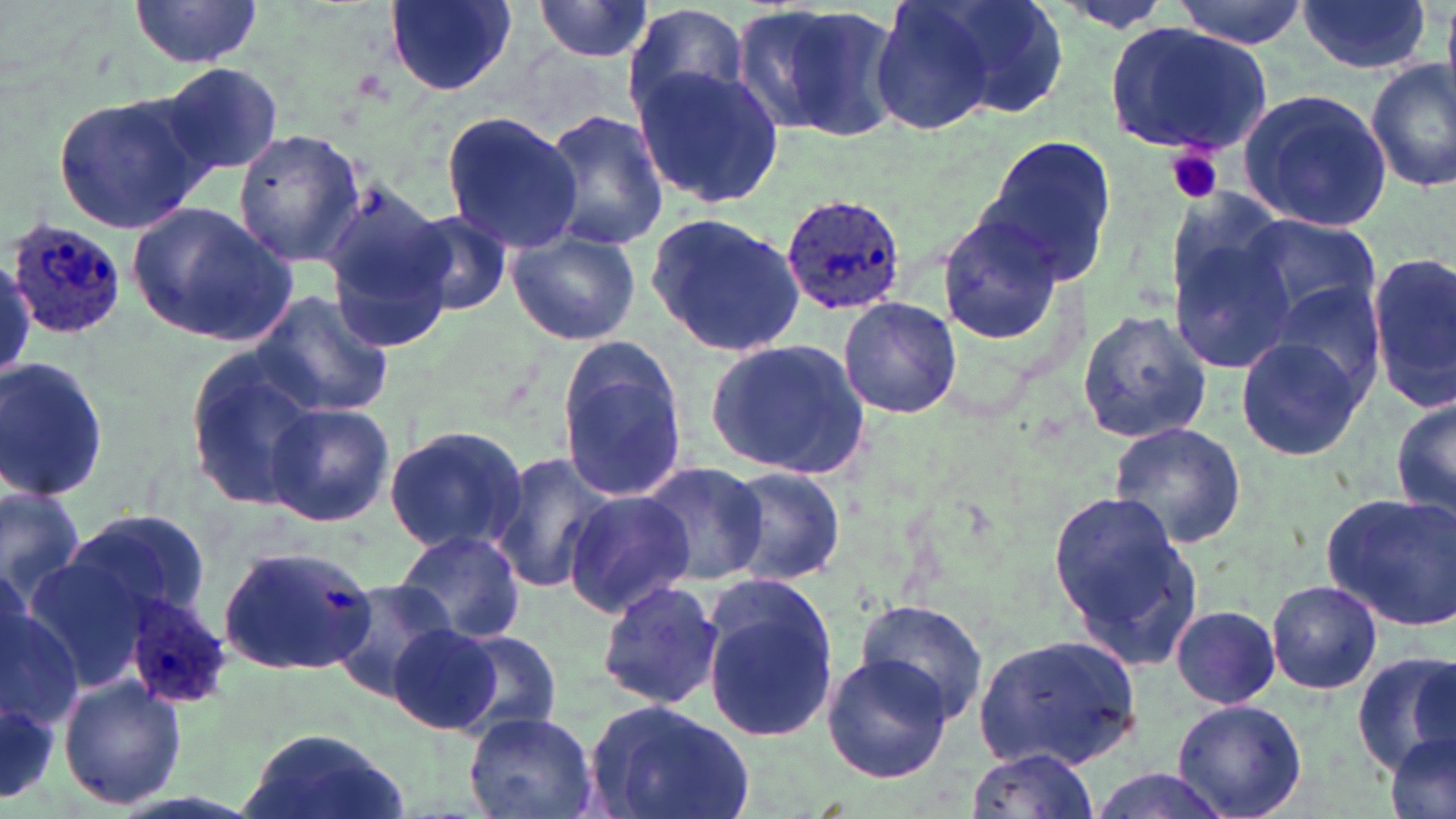

Approximate bounding boxes as (x1,y1)-(x2,y2) corner pairs in pixels. Plasmodium ovale-infected red blood cell locations: (779,193)-(907,320), (4,215)-(127,339), (119,591)-(230,711). Platelet locations: (1167,148)-(1223,204). Uninfected red blood cell locations: (932,0)-(1069,121), (1171,0)-(1312,47), (1296,0)-(1432,73), (384,1)-(517,96), (531,1)-(657,62), (871,1)-(1000,136), (129,2)-(263,69), (743,3)-(900,142), (624,5)-(751,123), (1106,23)-(1272,157), (1366,57)-(1456,193), (154,62)-(288,178), (632,64)-(782,207), (1238,89)-(1394,232), (51,90)-(214,238), (541,109)-(668,253), (441,112)-(588,252), (232,128)-(366,267), (974,133)-(1118,287), (318,177)-(450,323), (129,200)-(296,345), (932,209)-(1067,347), (404,210)-(512,317), (644,211)-(806,359), (1167,214)-(1299,374), (1237,214)-(1383,340), (505,228)-(643,346), (1368,250)-(1456,409), (1255,283)-(1386,405), (249,290)-(395,422), (838,297)-(961,419), (1076,306)-(1212,445), (1234,335)-(1368,463), (553,336)-(689,503), (704,338)-(872,480), (182,349)-(327,512), (0,357)-(110,505), (1390,391)-(1455,525), (265,402)-(395,527), (1107,421)-(1247,549), (384,425)-(528,557), (487,450)-(621,596), (638,460)-(769,585), (721,467)-(847,585), (0,482)-(88,603), (1047,487)-(1204,673), (561,490)-(695,616), (1320,490)-(1456,631), (62,508)-(210,629), (394,528)-(526,645), (216,545)-(378,678), (698,577)-(842,745), (595,579)-(725,709), (1266,579)-(1383,695), (329,580)-(458,701), (853,598)-(989,725), (2,602)-(82,744), (1169,605)-(1285,709), (389,621)-(502,735), (444,628)-(565,737), (973,632)-(1145,770), (1351,648)-(1455,774), (822,651)-(954,784), (59,679)-(185,809), (583,698)-(756,819), (1171,699)-(1309,819), (464,708)-(598,818), (234,729)-(408,819), (1381,733)-(1454,818), (964,748)-(1100,817), (1083,768)-(1236,819). Slide-level diagnosis: Plasmodium ovale. May-Grünwald-Giemsa-stained preparation. Thin blood smear. Image is 1456×819 pixels. Single field of view. 1000x magnification. Optical microscopy.